Identify the blood parasite species.
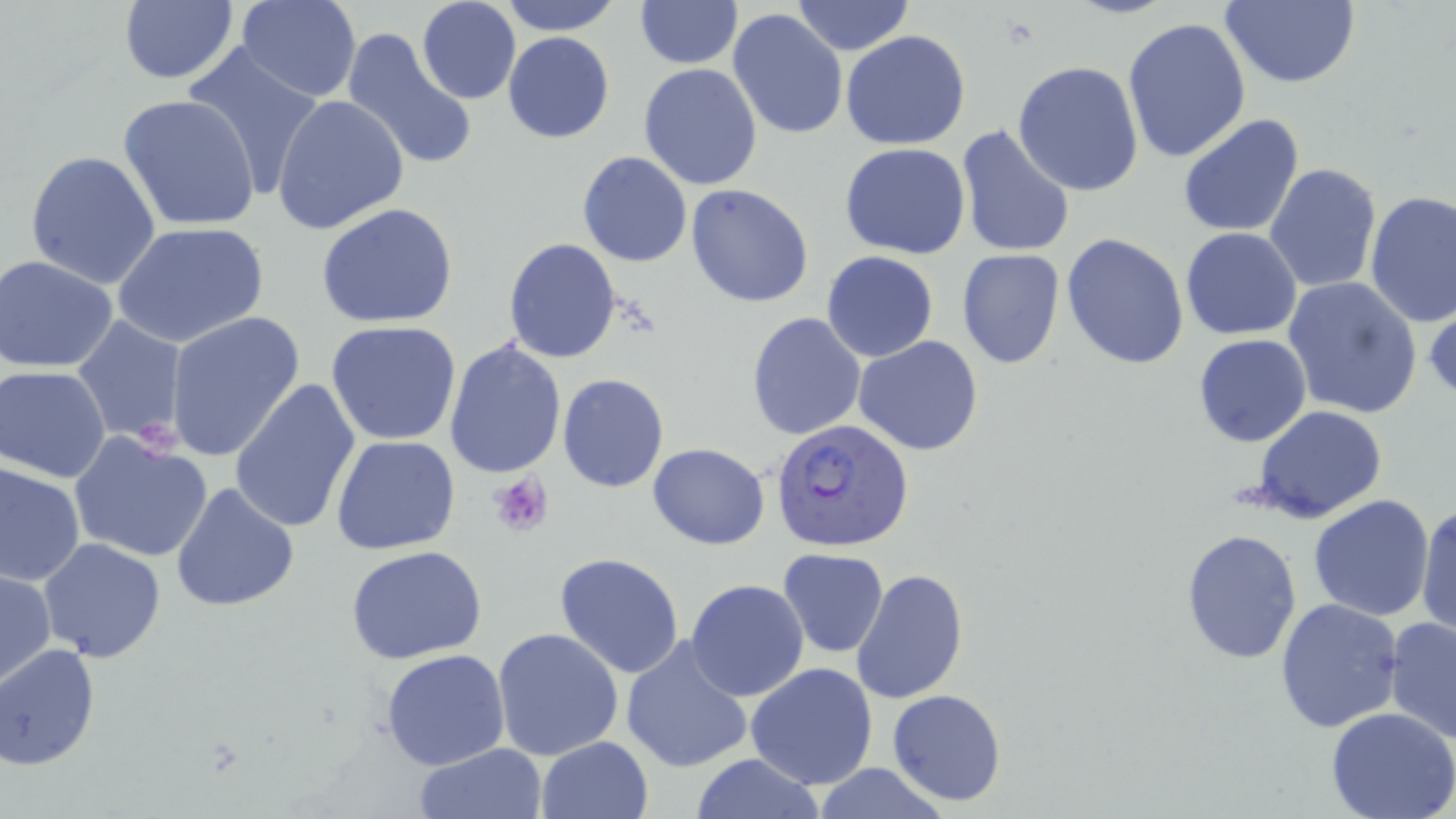
Plasmodium falciparum.

Approximate bounding boxes as (x1, y1, x2, y2) in pixels. Platelet locations: (488, 473, 553, 536). Uninfected red blood cell locations: (117, 0, 238, 86), (236, 0, 361, 102), (497, 0, 623, 35), (790, 0, 916, 54), (1218, 0, 1361, 89), (415, 1, 522, 104), (633, 1, 742, 69), (727, 9, 849, 141), (1122, 17, 1252, 164), (341, 29, 478, 174), (840, 30, 971, 151), (503, 32, 615, 143), (179, 42, 328, 197), (1013, 60, 1145, 196), (638, 62, 762, 190), (119, 94, 261, 234), (270, 95, 409, 234), (1177, 113, 1305, 238), (954, 124, 1076, 260), (840, 143, 971, 259), (25, 149, 164, 290), (577, 150, 693, 268), (1263, 162, 1382, 294), (575, 163, 800, 282), (686, 184, 814, 307), (1365, 191, 1456, 327), (315, 203, 459, 329), (112, 222, 269, 349), (1181, 227, 1302, 341), (1061, 232, 1189, 371), (504, 238, 622, 363), (956, 248, 1065, 368), (822, 251, 938, 362), (0, 255, 119, 374), (1283, 276, 1422, 420), (1424, 293, 1456, 406), (166, 310, 305, 461), (747, 313, 867, 442), (71, 317, 188, 445), (326, 320, 461, 446), (1192, 334, 1313, 447), (853, 335, 985, 457), (443, 339, 567, 480), (1, 365, 114, 482), (557, 373, 670, 493), (229, 376, 362, 535), (1251, 406, 1388, 520), (70, 431, 213, 564), (330, 436, 460, 556), (647, 443, 770, 549), (1, 462, 85, 585), (171, 480, 299, 612), (1308, 495, 1435, 622), (1415, 501, 1454, 637), (1180, 528, 1302, 665), (38, 538, 167, 661), (347, 546, 487, 664), (777, 548, 889, 658), (554, 553, 686, 679), (1, 567, 55, 688), (850, 568, 968, 705), (685, 579, 810, 702), (1275, 598, 1404, 734), (1384, 616, 1456, 744), (492, 628, 624, 760), (619, 637, 754, 775), (0, 644, 100, 769), (380, 648, 510, 770), (745, 663, 877, 790), (887, 689, 1006, 807), (1326, 707, 1456, 819), (536, 736, 653, 819), (413, 742, 548, 819), (686, 754, 829, 818), (807, 763, 954, 819). Plasmodium falciparum-infected red blood cell locations: (772, 418, 915, 554). Thin blood smear. May-Grünwald-Giemsa stain. Image is 1456×819 pixels. Single field of view. Light microscopy. Captured at 1000x magnification.